Locate every blood parasite and identify its species.
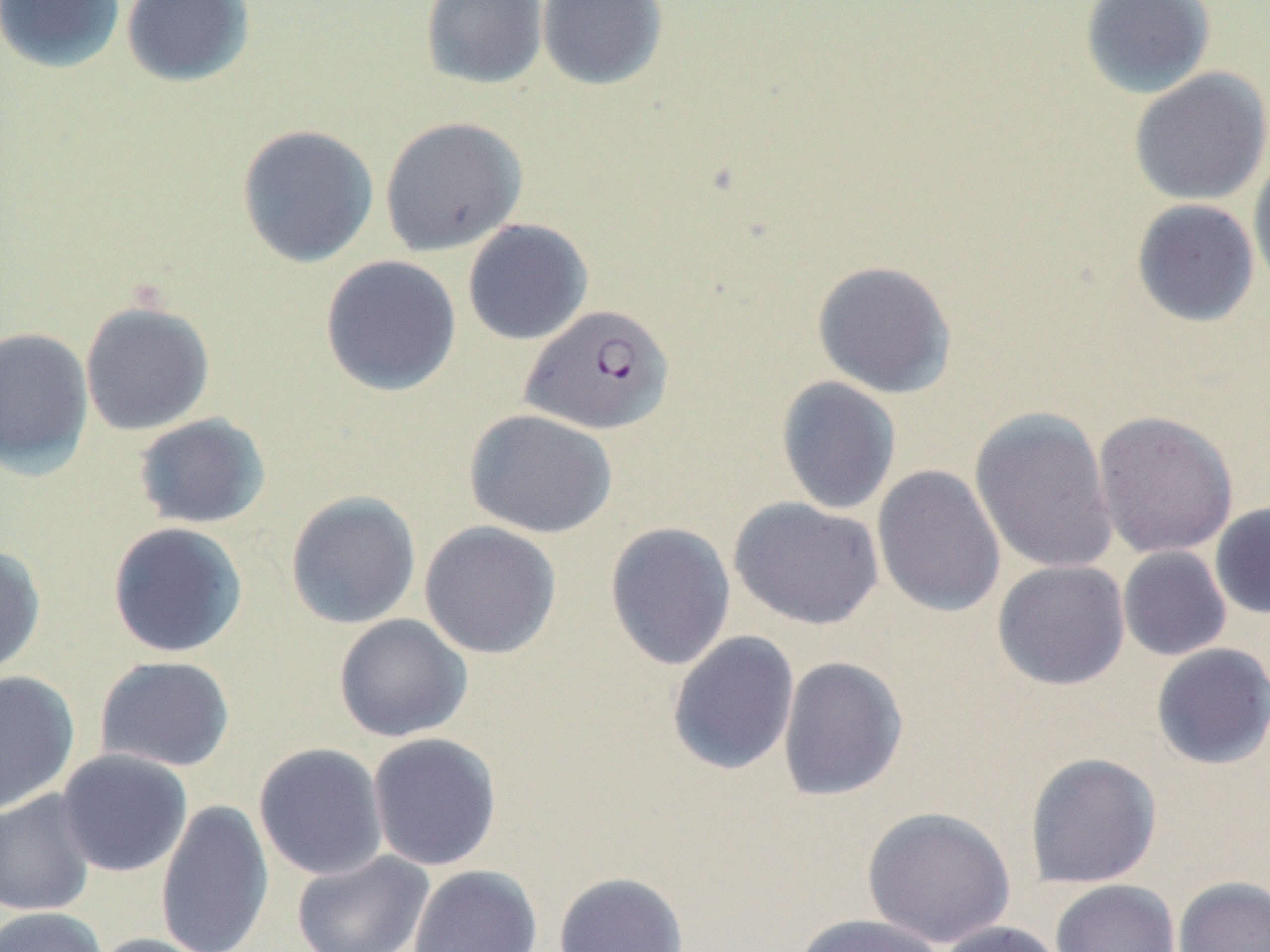
Approximate bounding boxes as (x1, y1, x2, y2) in pixels.
Plasmodium falciparum-infected red blood cells: (520, 303, 675, 436).
No Plasmodium ovale, Plasmodium malariae, Plasmodium vivax, Babesia divergens, or Trypanosoma brucei observed.

{
  "slide_level_diagnosis": "Plasmodium falciparum",
  "preparation": "thin blood film",
  "modality": "light microscopy",
  "stain": "May-Grünwald-Giemsa",
  "field_of_view": "single",
  "uninfected_red_blood_cell_locations": "approximate bounding boxes as (x1, y1, x2, y2) in pixels: (0, 0, 126, 73), (121, 0, 255, 87), (419, 0, 548, 90), (536, 0, 668, 91), (1079, 0, 1216, 99), (1129, 68, 1270, 206), (379, 116, 528, 257), (236, 123, 379, 267), (1247, 153, 1270, 295), (1131, 199, 1260, 328), (462, 218, 593, 346), (320, 255, 461, 397), (811, 260, 958, 399), (79, 300, 216, 436), (0, 326, 94, 479), (775, 376, 901, 515), (969, 406, 1118, 575), (464, 408, 616, 538), (1093, 410, 1239, 559), (132, 413, 271, 530), (872, 465, 1006, 619), (285, 491, 421, 629), (728, 497, 885, 630), (1209, 501, 1270, 620), (419, 520, 562, 660), (107, 521, 249, 659), (604, 522, 736, 670), (0, 544, 46, 679), (1117, 546, 1232, 661), (992, 560, 1131, 691), (334, 613, 472, 742), (666, 631, 800, 776), (1150, 643, 1270, 771), (94, 655, 236, 773), (777, 655, 909, 802), (0, 671, 80, 815), (367, 732, 503, 871), (253, 743, 388, 881), (55, 749, 193, 877), (1024, 752, 1162, 889), (0, 790, 97, 917), (155, 799, 274, 952), (862, 806, 1017, 948), (291, 850, 436, 952), (408, 864, 542, 952), (553, 871, 689, 952), (1172, 875, 1270, 952), (1051, 879, 1181, 952), (0, 906, 108, 952), (788, 913, 948, 952), (933, 920, 1067, 952), (87, 933, 218, 952)",
  "image_size": "1270×952 pixels",
  "magnification": "1000x"
}